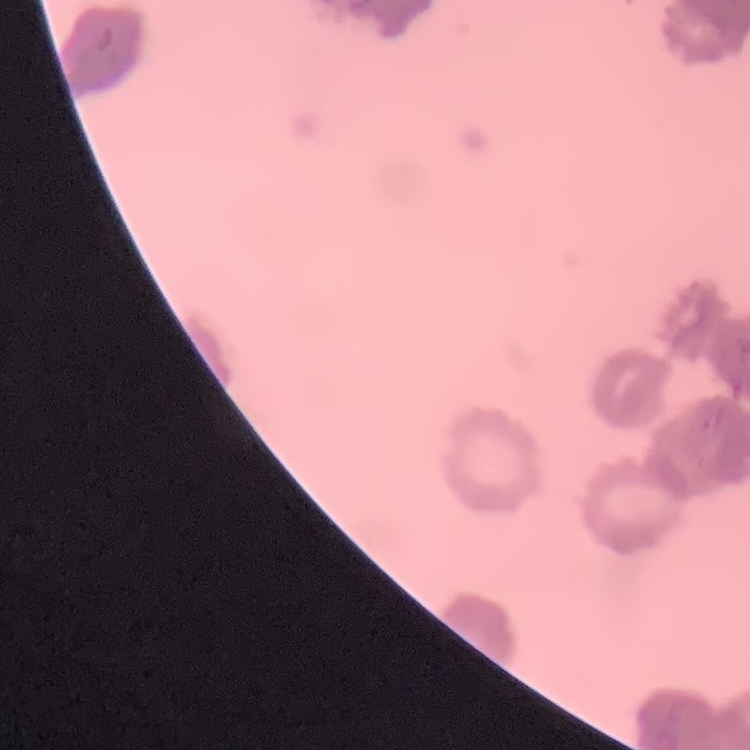

The erythrocytes show rouleaux formation. One tile cut from a larger photomicrograph. Stained with either Field's or Giemsa. Thin blood smear.